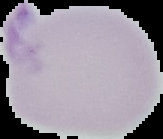

Summary:
  - Image type: segmented cell region with the area outside set to black
  - Preparation: thin blood film
  - Malaria status: uninfected
  - Image size: 163×139 pixels